Draw a bounding box around every leukocyte (white blood cell).
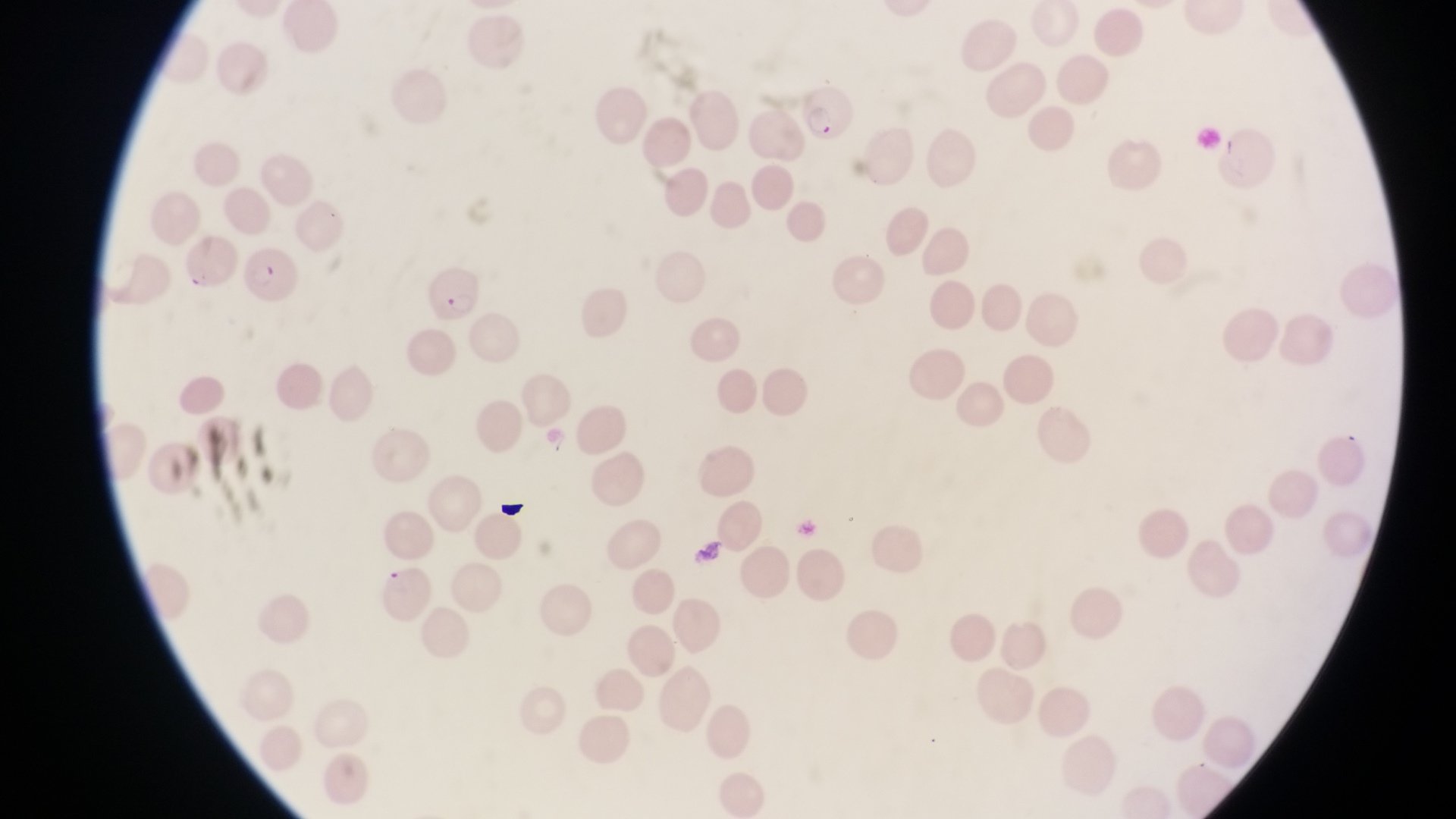

No leukocytes observed.

Approximate bounding boxes as {left, top, right, bottom} in pixels.
Summary:
  - Artifact (platelet-like body, stain precipitate, or debris) locations: {497, 497, 532, 527}, {693, 535, 728, 574}
  - Parasitised red blood cell locations: {789, 82, 853, 143}, {246, 246, 299, 307}, {416, 261, 476, 328}
  - Image size: 1456×819 pixels
  - Capture: smartphone photograph through the eyepiece of an Olympus CX-23 microscope
  - Magnification: 1000x
  - Preparation: thin blood smear
  - Field of view: single
  - Country: Uganda